Report the malaria status of this cell.
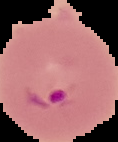
It is parasitized.

image size = 118×142 pixels
image type = segmented cell region with the area outside set to black
preparation = thin blood smear